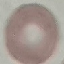
Summary:
  - Result: no malaria parasites seen
  - Stain: Giemsa
  - Image type: cell patch, automatically extracted from a larger field of view and resized to 64 × 64 pixels
  - Capture: smartphone camera at the microscope eyepiece
  - Preparation: thin smear